Classify this cell by malaria status.
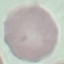

It is uninfected.

Automatically extracted cell patch, resized to 64 × 64 pixels. Acquired by smartphone through the microscope eyepiece. Thin blood film. Giemsa stain.